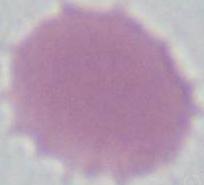
identification: red blood cell
magnification: 1000x
modality: photomicrograph